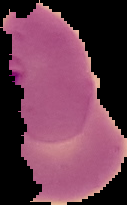 From a thin blood smear. Image is 127×205 pixels. Result: malaria parasites detected. Segmented cell region on a black background.